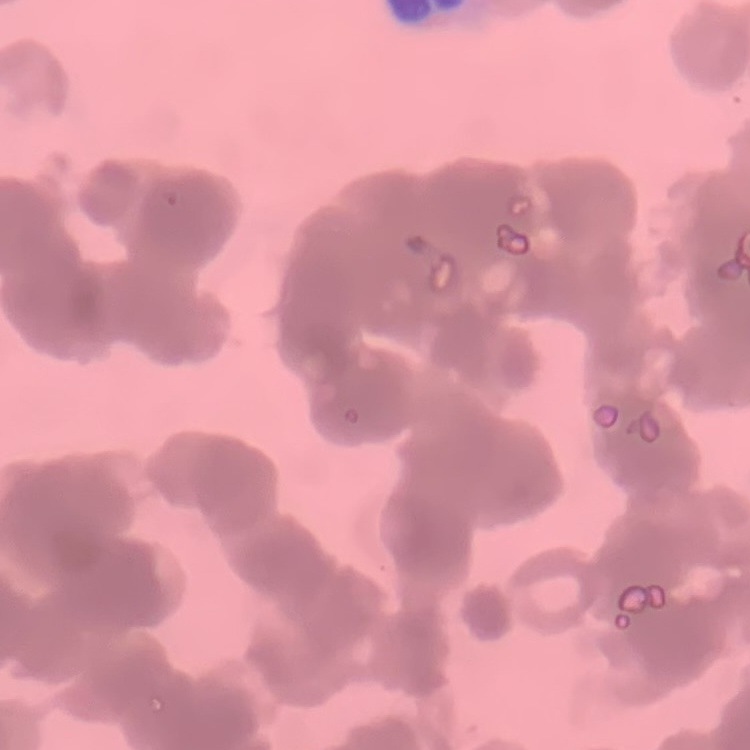
{
  "red_blood_cell_morphology": "rouleaux formation",
  "stain": "Field's or Giemsa",
  "preparation": "thin peripheral smear",
  "image_type": "one tile cut from a larger photomicrograph"
}